Give the preparation type.
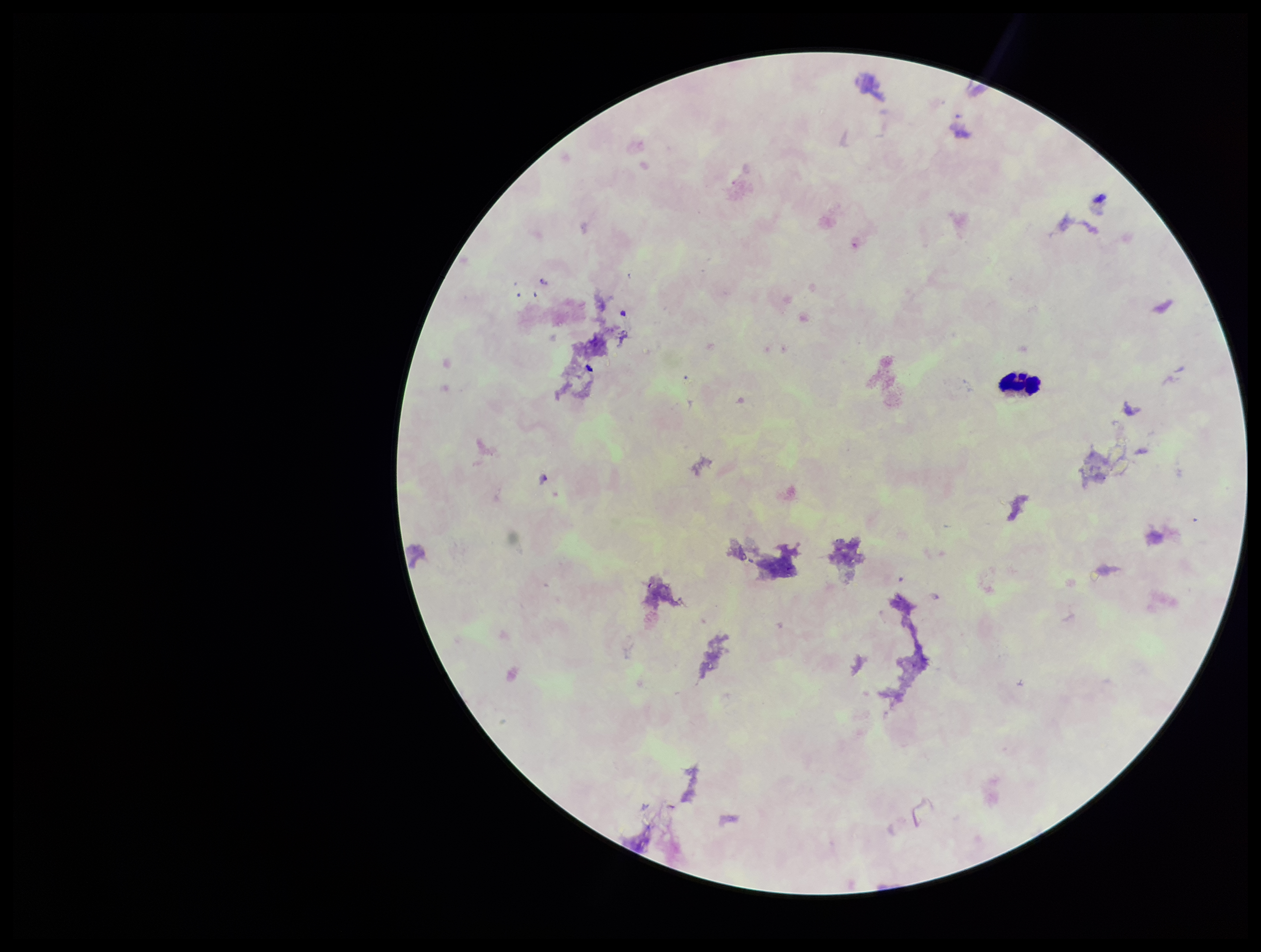

Thick.

Giemsa stain. Parasite count: 0. Plasmodium parasites: none detected. Leukocyte count: 1. Patient malaria status: negative. Image is 1261×952 pixels. Smartphone photograph taken through the eyepiece of a microscope. Single field of view.